Comment on the morphology of the red blood cells.
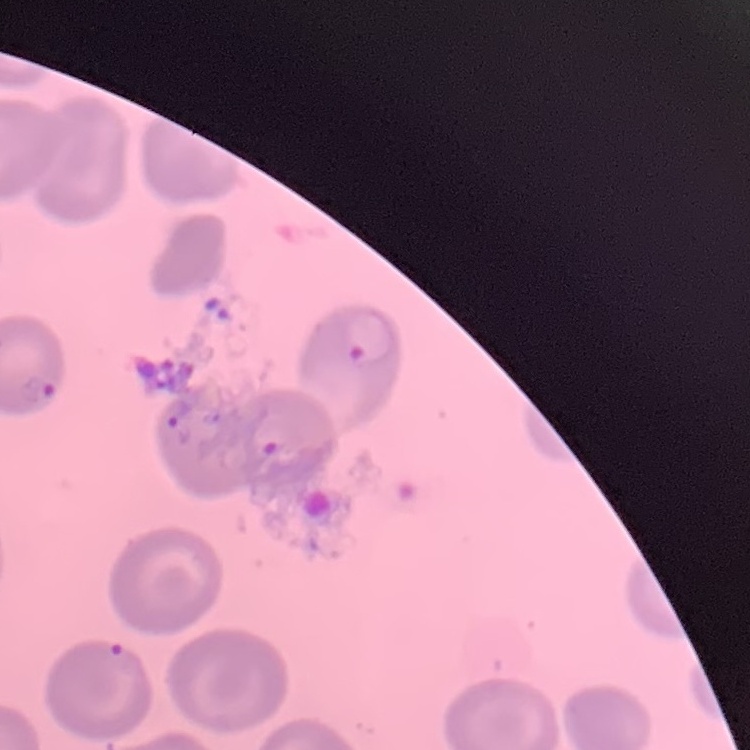

No rouleaux formation.

Summary:
  - Stain: Field's or Giemsa
  - Preparation: thin blood film
  - Image type: one tile cut from a larger photomicrograph